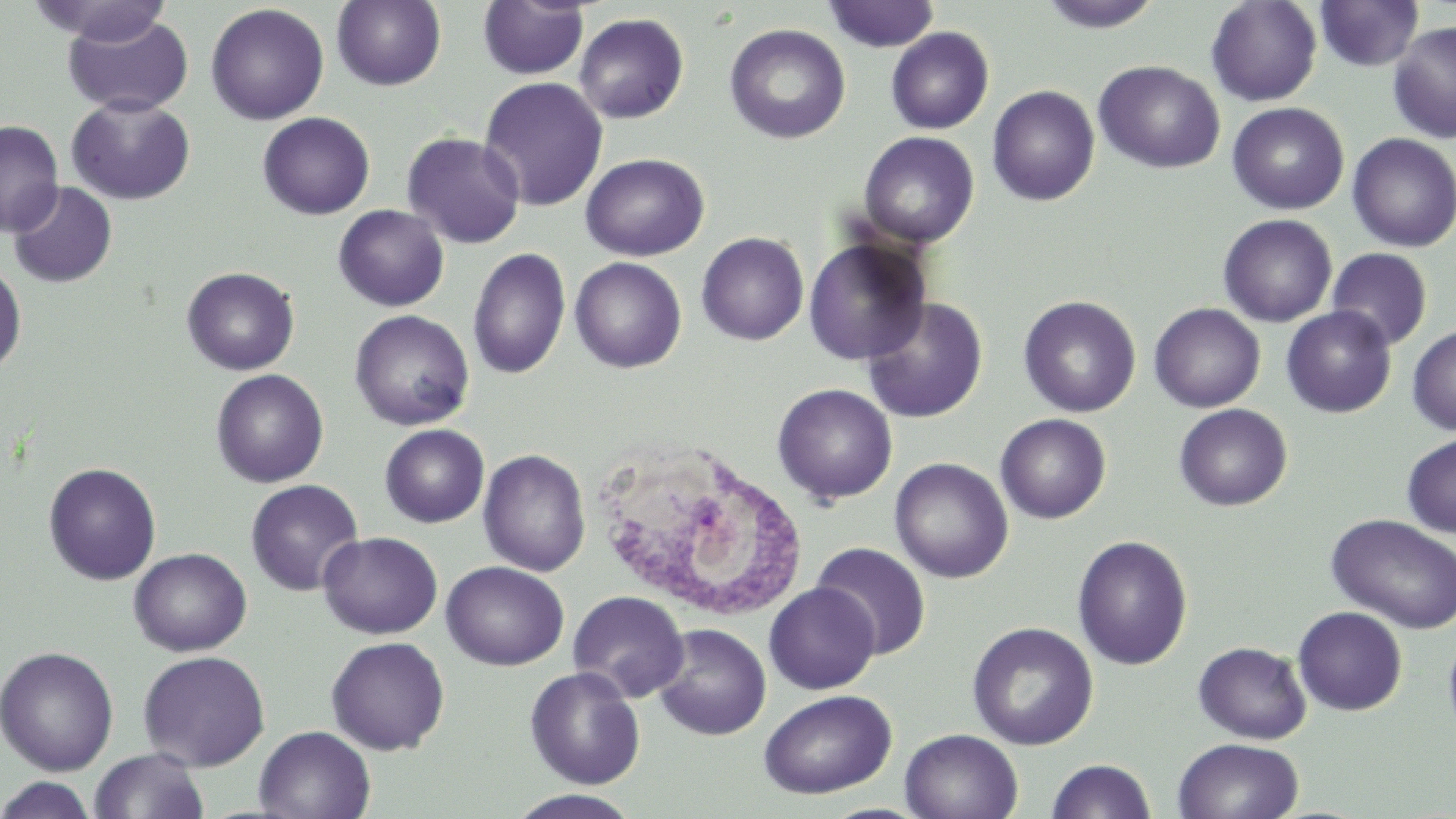

Summary:
  - Coordinate format: approximate bounding boxes as (x1, y1, x2, y2) in pixels
  - Uninfected red blood cell locations: (27, 0, 175, 46), (331, 0, 447, 91), (1036, 0, 1165, 33), (1206, 0, 1322, 106), (1314, 0, 1424, 72), (477, 1, 589, 80), (822, 1, 940, 52), (205, 3, 329, 125), (64, 13, 195, 117), (573, 13, 689, 123), (1387, 21, 1456, 143), (724, 24, 851, 144), (886, 27, 994, 134), (1094, 60, 1225, 174), (478, 76, 609, 211), (987, 85, 1100, 206), (66, 95, 195, 205), (1227, 102, 1349, 215), (257, 112, 375, 219), (0, 120, 64, 236), (401, 131, 526, 249), (858, 131, 979, 247), (1347, 133, 1456, 252), (580, 153, 709, 261), (8, 181, 117, 288), (333, 204, 449, 312), (1217, 214, 1338, 327), (696, 232, 809, 345), (803, 237, 932, 365), (467, 247, 571, 380), (1327, 247, 1433, 351), (569, 256, 687, 373), (0, 260, 27, 375), (182, 267, 299, 375), (861, 296, 988, 423), (1018, 296, 1141, 417), (1149, 302, 1266, 413), (1281, 306, 1396, 418), (349, 310, 474, 431), (1407, 324, 1456, 435), (210, 369, 329, 488), (772, 382, 898, 505), (1174, 404, 1292, 511), (995, 414, 1111, 523), (379, 424, 489, 527), (1401, 432, 1456, 538), (478, 449, 591, 577), (889, 457, 1014, 583), (43, 462, 161, 585), (245, 479, 364, 596), (1327, 513, 1456, 634), (318, 531, 443, 639), (1072, 535, 1193, 670), (811, 542, 932, 659), (128, 547, 252, 656), (441, 561, 569, 670), (763, 582, 880, 694), (568, 590, 689, 702), (1293, 606, 1407, 715), (966, 621, 1099, 750), (652, 624, 772, 741), (1443, 629, 1456, 743), (326, 635, 450, 755), (1193, 641, 1312, 744), (0, 645, 120, 776), (137, 650, 270, 771), (524, 666, 646, 790), (758, 689, 897, 799), (254, 726, 376, 819), (900, 729, 1023, 819), (1172, 737, 1304, 819), (88, 748, 210, 819), (1046, 759, 1157, 818), (0, 775, 97, 819), (506, 789, 644, 819)
  - White blood cell locations: (593, 443, 809, 622)
  - Slide-level diagnosis: negative for blood parasites
  - Stain: May-Grünwald-Giemsa
  - Image size: 1456×819 pixels
  - Preparation: thin blood film
  - Field of view: single
  - Magnification: 1000x
  - Modality: optical microscopy